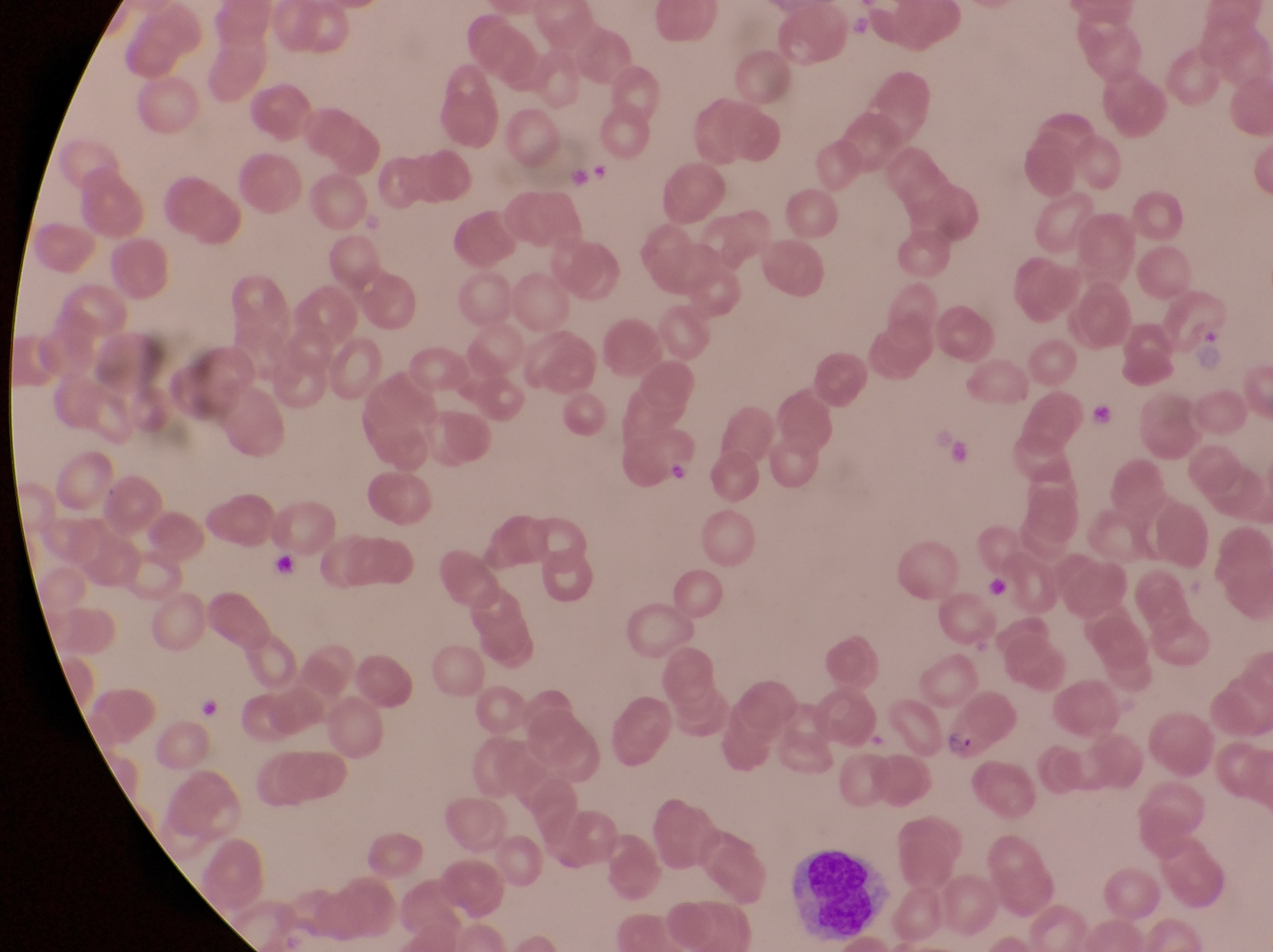
{
  "parasitised_red_blood_cell_locations": "approximate bounding boxes as (left, top, right, bottom) in pixels: (939, 702, 992, 770)",
  "field_of_view": "single",
  "image_size": "1273×952 pixels",
  "magnification": "1000x",
  "artifact_platelet_like_body_stain_precipitate_or_debris_locations": "approximate bounding boxes as (left, top, right, bottom) in pixels: (1086, 395, 1125, 430), (262, 537, 302, 580), (981, 570, 1018, 613)",
  "capture": "smartphone photograph through the eyepiece of an Olympus CX-23 microscope",
  "leukocyte_locations": "approximate bounding boxes as (left, top, right, bottom) in pixels: (786, 851, 879, 929)",
  "trophozoite_locations": "approximate bounding boxes as (left, top, right, bottom) in pixels: (582, 160, 625, 199)",
  "country": "Uganda",
  "preparation": "thin blood smear"
}